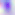

{
  "identification": "Toxoplasma gondii",
  "modality": "photomicrograph",
  "magnification": "400x"
}